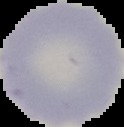

Cell region segmented out of the field of view; the surrounding area is masked to black. From a thin blood film. Image is 124×127 pixels. Result: negative for malaria parasites.